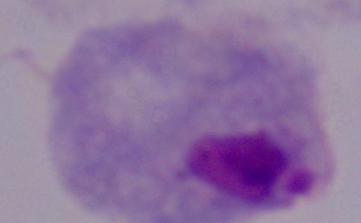 Captured at 1000x magnification. Micrograph. A trichomonad is seen.